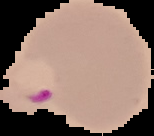
Result: malaria parasites detected. Segmented cell region on a black background. From a thin blood film. Image is 154×136 pixels.